Comment on the morphology of the red blood cells.
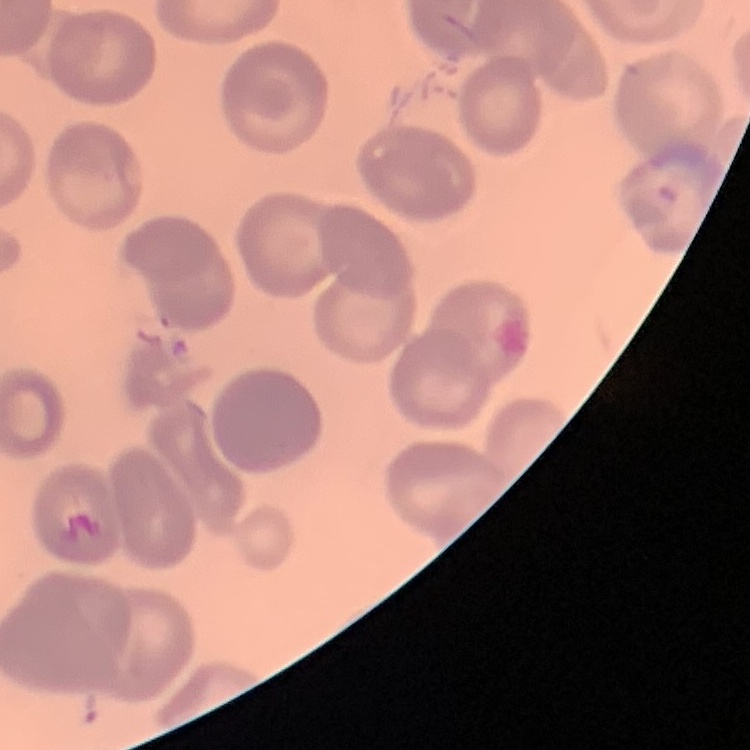
No rouleaux formation.

stain = Field's or Giemsa
preparation = thin blood smear
image type = square crop of a larger photomicrograph